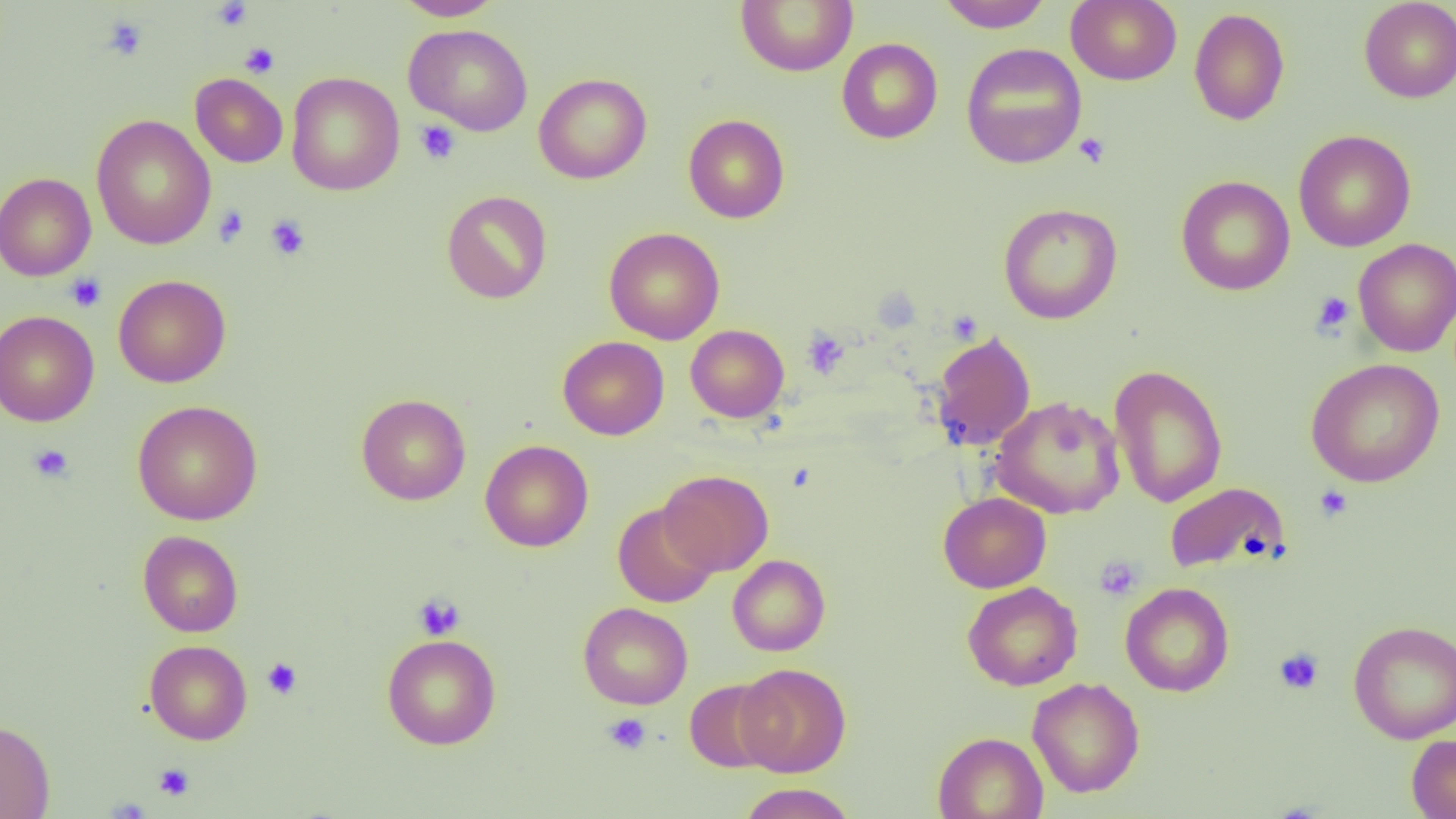 Approximate bounding boxes as [x1, y1, x2, y2] in pixels. Uninfected red blood cell locations: [393, 0, 502, 21], [735, 0, 857, 77], [936, 0, 1055, 32], [1066, 0, 1182, 85], [1359, 0, 1456, 103], [1188, 7, 1290, 126], [404, 24, 533, 136], [837, 38, 943, 144], [961, 42, 1087, 169], [285, 72, 405, 196], [190, 73, 288, 167], [533, 73, 652, 184], [683, 114, 790, 223], [91, 115, 216, 249], [1293, 129, 1416, 252], [0, 172, 97, 281], [1176, 175, 1295, 296], [441, 190, 552, 304], [998, 203, 1123, 324], [604, 227, 725, 344], [1353, 238, 1456, 356], [113, 274, 231, 388], [0, 310, 100, 427], [685, 324, 790, 422], [931, 330, 1036, 450], [558, 336, 669, 440], [1305, 357, 1445, 487], [1109, 364, 1228, 508], [356, 394, 471, 505], [990, 395, 1125, 519], [132, 400, 263, 525], [480, 439, 594, 552], [659, 469, 773, 577], [1164, 482, 1291, 574], [938, 492, 1051, 593], [612, 502, 719, 608], [138, 530, 244, 637], [727, 555, 830, 656], [962, 582, 1083, 691], [1120, 582, 1234, 697], [578, 602, 693, 709], [1348, 620, 1456, 744], [382, 633, 501, 750], [144, 640, 252, 745], [736, 663, 851, 777], [1027, 677, 1145, 798], [684, 678, 781, 773], [0, 719, 55, 819], [933, 731, 1048, 819], [1406, 734, 1456, 819], [737, 783, 857, 819]. Platelet locations: [212, 1, 253, 31], [102, 15, 149, 61], [240, 42, 279, 78], [414, 120, 461, 165], [1074, 132, 1110, 168], [213, 206, 249, 247], [265, 215, 310, 260], [66, 273, 106, 312], [1311, 291, 1355, 335], [802, 329, 850, 379], [28, 444, 74, 483], [1314, 485, 1353, 522], [1094, 556, 1143, 600], [412, 593, 465, 640], [1274, 648, 1324, 695], [261, 657, 302, 699], [603, 713, 651, 755], [154, 763, 195, 801]. Slide-level diagnosis: negative for blood parasites. Image is 1456×819 pixels. Thin blood smear. Single field of view. Captured at 1000x magnification. Light microscopy.